Look for Plasmodium parasites.
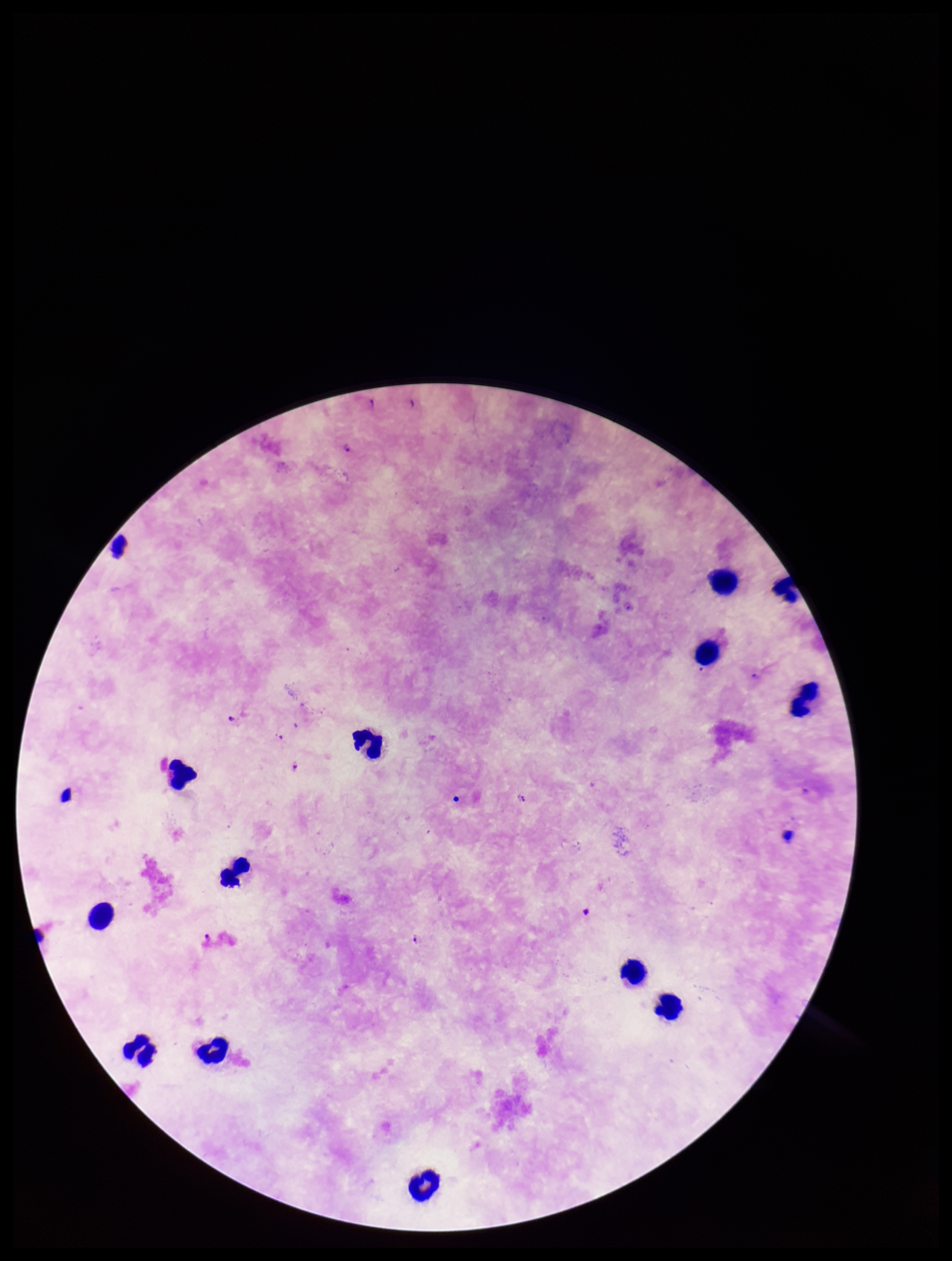

Identified.

Summary:
  - Patient malaria status: positive
  - Parasite count: 7
  - Preparation: thick blood smear
  - Leukocyte count: 13
  - Image size: 952×1261 pixels
  - Stain: Giemsa
  - Species reported for this patient: Plasmodium falciparum
  - Field of view: single
  - Capture: smartphone photograph through the microscope eyepiece